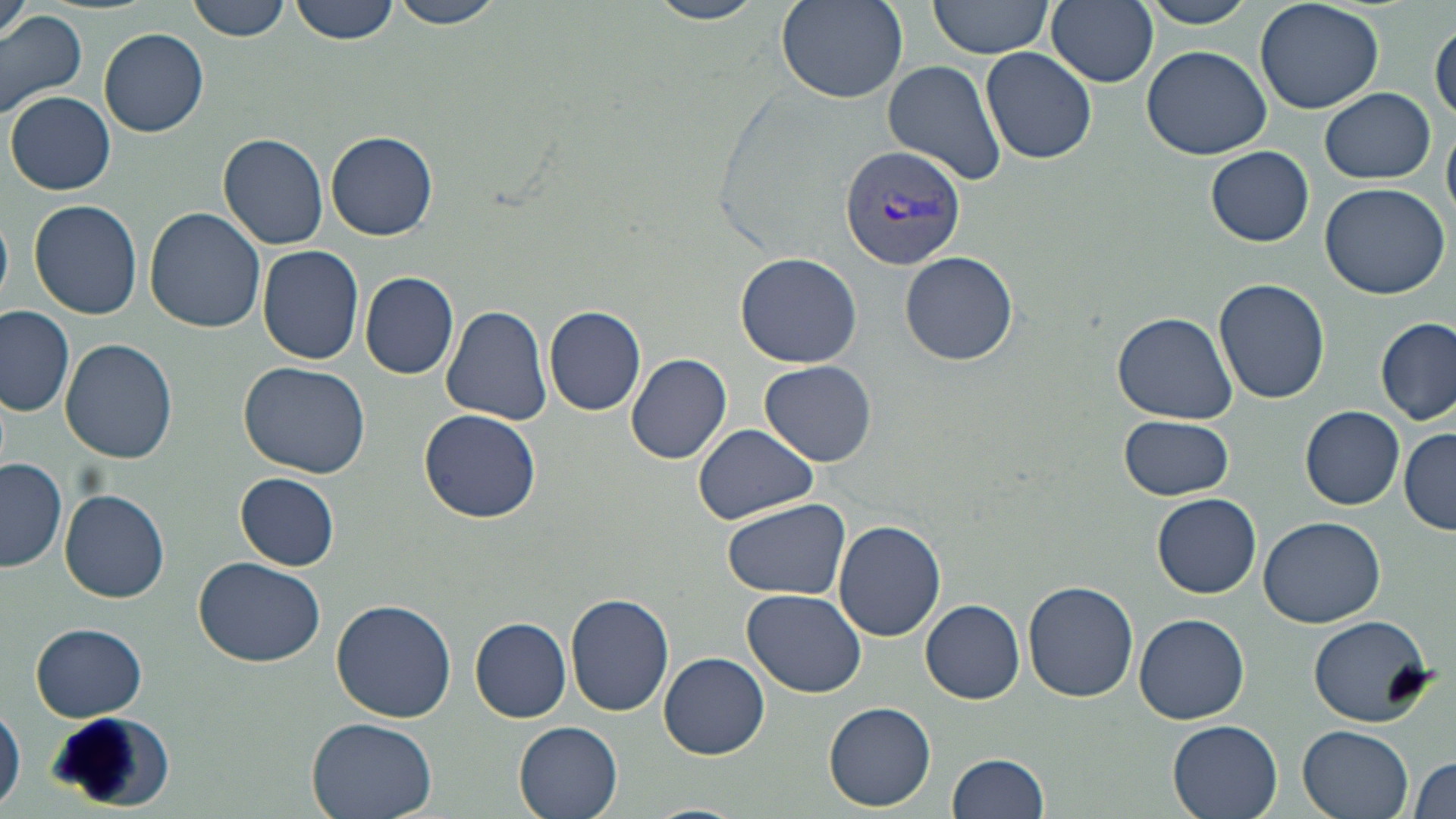
Summary:
  - Coordinate format: approximate bounding boxes as named x1/y1/x2/y2 corners in pixels
  - Uninfected red blood cell locations: (x1=2, y1=0, x2=31, y2=45), (x1=187, y1=0, x2=292, y2=42), (x1=291, y1=0, x2=399, y2=45), (x1=392, y1=0, x2=506, y2=30), (x1=645, y1=0, x2=769, y2=25), (x1=924, y1=0, x2=1057, y2=63), (x1=1045, y1=0, x2=1158, y2=88), (x1=1135, y1=0, x2=1262, y2=28), (x1=1254, y1=0, x2=1382, y2=113), (x1=775, y1=1, x2=908, y2=105), (x1=0, y1=6, x2=87, y2=118), (x1=1431, y1=20, x2=1455, y2=124), (x1=99, y1=28, x2=208, y2=137), (x1=1142, y1=45, x2=1274, y2=162), (x1=981, y1=46, x2=1097, y2=165), (x1=882, y1=59, x2=1006, y2=187), (x1=1321, y1=88, x2=1435, y2=183), (x1=6, y1=92, x2=115, y2=195), (x1=325, y1=131, x2=438, y2=240), (x1=218, y1=135, x2=329, y2=250), (x1=1206, y1=146, x2=1313, y2=246), (x1=1320, y1=181, x2=1451, y2=300), (x1=27, y1=199, x2=143, y2=319), (x1=145, y1=208, x2=264, y2=332), (x1=0, y1=212, x2=12, y2=305), (x1=259, y1=246, x2=365, y2=365), (x1=735, y1=252, x2=861, y2=368), (x1=900, y1=252, x2=1018, y2=365), (x1=359, y1=271, x2=459, y2=379), (x1=1214, y1=277, x2=1330, y2=405), (x1=0, y1=305, x2=76, y2=417), (x1=441, y1=305, x2=553, y2=424), (x1=544, y1=305, x2=647, y2=417), (x1=1111, y1=311, x2=1238, y2=424), (x1=1376, y1=316, x2=1454, y2=425), (x1=62, y1=338, x2=178, y2=464), (x1=626, y1=353, x2=733, y2=466), (x1=761, y1=360, x2=876, y2=466), (x1=239, y1=361, x2=370, y2=479), (x1=1300, y1=405, x2=1405, y2=508), (x1=420, y1=409, x2=543, y2=524), (x1=1120, y1=414, x2=1235, y2=501), (x1=693, y1=423, x2=817, y2=524), (x1=1400, y1=427, x2=1456, y2=535), (x1=1, y1=457, x2=68, y2=573), (x1=237, y1=474, x2=339, y2=569), (x1=60, y1=489, x2=170, y2=603), (x1=1153, y1=493, x2=1262, y2=598), (x1=722, y1=498, x2=852, y2=601), (x1=1258, y1=515, x2=1386, y2=626), (x1=833, y1=520, x2=946, y2=643), (x1=194, y1=557, x2=326, y2=668), (x1=1023, y1=580, x2=1139, y2=702), (x1=743, y1=588, x2=869, y2=695), (x1=565, y1=593, x2=676, y2=717), (x1=331, y1=597, x2=457, y2=721), (x1=921, y1=599, x2=1025, y2=704), (x1=1135, y1=613, x2=1249, y2=724), (x1=470, y1=616, x2=572, y2=723), (x1=1309, y1=616, x2=1433, y2=724), (x1=30, y1=621, x2=146, y2=720), (x1=660, y1=653, x2=769, y2=757), (x1=825, y1=702, x2=936, y2=810), (x1=1, y1=704, x2=25, y2=814), (x1=306, y1=718, x2=438, y2=819), (x1=1169, y1=719, x2=1284, y2=819), (x1=515, y1=720, x2=624, y2=819), (x1=1296, y1=723, x2=1416, y2=819), (x1=947, y1=753, x2=1049, y2=819), (x1=1409, y1=754, x2=1456, y2=819), (x1=642, y1=802, x2=751, y2=819)
  - Plasmodium vivax-infected red blood cell locations: (x1=839, y1=144, x2=966, y2=271)
  - Slide-level diagnosis: Plasmodium vivax
  - Field of view: single
  - Image size: 1456×819 pixels
  - Magnification: 1000x
  - Modality: light microscopy
  - Preparation: thin blood smear
  - Stain: May-Grünwald-Giemsa